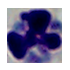

magnification = 1000x
modality = photomicrograph
identification = leukocyte